Give the extent of all Babesia divergens-infected red blood cells.
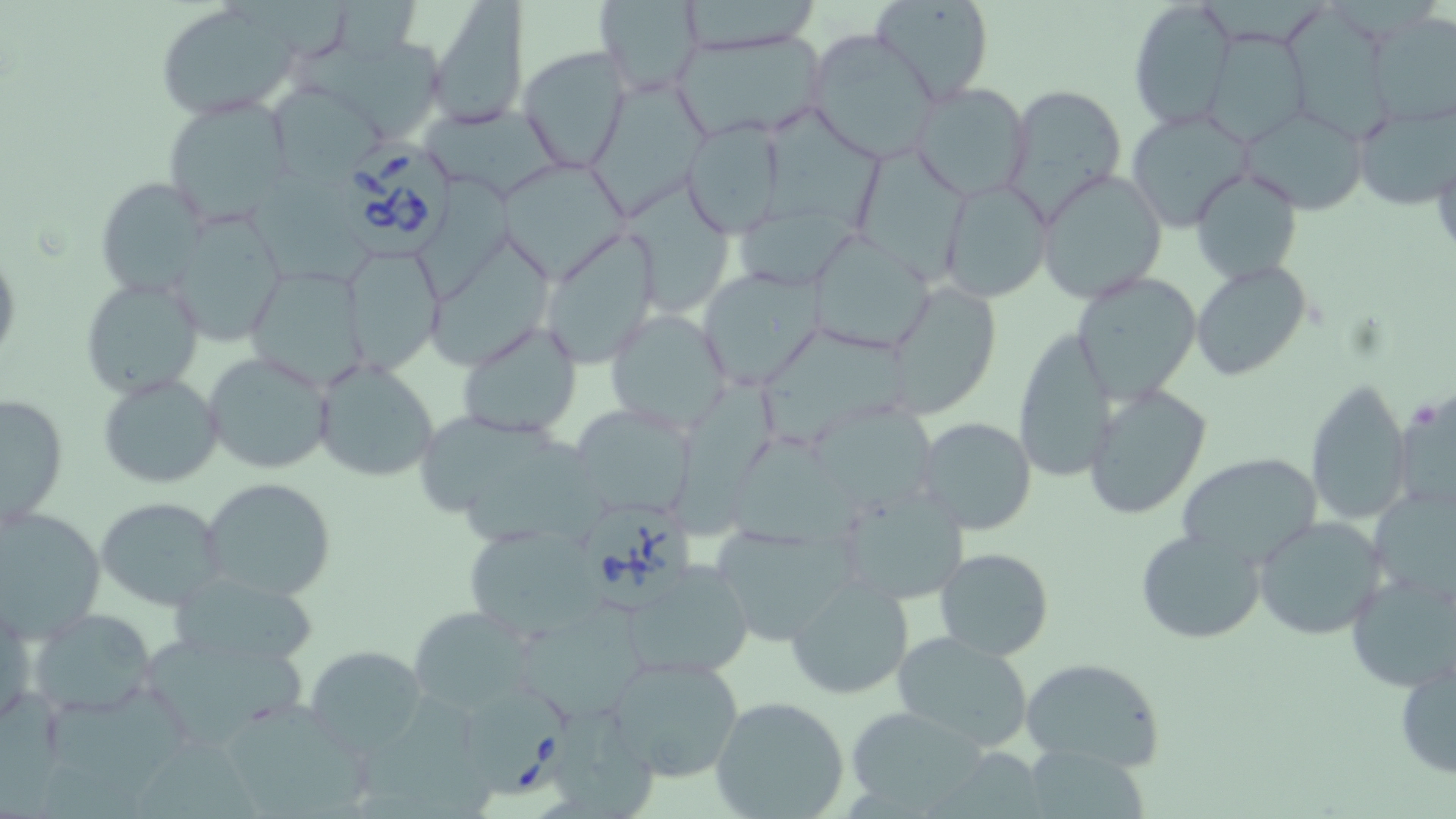
Approximate bounding boxes as (x1,y1)-(x2,y2) corner pairs in pixels.
Babesia divergens-infected red blood cells: (336,137)-(462,262), (580,501)-(702,614), (462,684)-(572,802).

Uninfected red blood cell locations: (427,0)-(530,130), (870,0)-(995,105), (223,1)-(351,59), (594,1)-(705,96), (678,1)-(821,52), (1126,1)-(1237,130), (153,3)-(302,118), (1280,11)-(1391,138), (1365,13)-(1455,127), (1203,29)-(1308,147), (673,30)-(830,141), (807,30)-(941,162), (518,44)-(631,171), (289,51)-(444,135), (269,82)-(387,182), (595,82)-(715,213), (909,82)-(1034,202), (1004,83)-(1128,217), (161,96)-(297,226), (1354,100)-(1455,208), (1239,105)-(1366,214), (1126,107)-(1255,230), (757,108)-(893,224), (682,119)-(785,237), (859,148)-(965,283), (500,158)-(630,278), (1035,168)-(1166,304), (1189,168)-(1304,284), (406,173)-(516,302), (248,175)-(376,288), (95,177)-(210,297), (623,181)-(734,313), (941,181)-(1057,307), (738,206)-(861,294), (164,207)-(289,346), (537,228)-(663,369), (807,230)-(937,355), (427,241)-(553,371), (340,245)-(440,372), (1190,259)-(1313,383), (242,264)-(372,392), (696,268)-(823,389), (1070,269)-(1203,404), (80,276)-(204,400), (882,279)-(1003,418), (626,293)-(816,418), (605,307)-(734,431), (456,322)-(582,441), (1013,327)-(1117,483), (751,328)-(906,453), (202,351)-(334,474), (312,358)-(440,484), (98,374)-(223,489), (670,378)-(779,536), (1304,378)-(1412,527), (1083,384)-(1213,520), (1392,386)-(1456,518), (1,391)-(69,528), (570,402)-(698,519), (811,407)-(943,510), (419,409)-(564,511), (915,416)-(1037,535), (732,437)-(866,546), (1176,453)-(1324,570), (201,476)-(338,601), (832,482)-(971,606), (1368,486)-(1455,603), (95,496)-(227,609), (0,505)-(107,639), (1253,515)-(1391,642), (707,520)-(854,646), (461,524)-(603,639), (1135,528)-(1266,645), (935,547)-(1054,661), (619,558)-(759,681), (1345,568)-(1456,693), (172,571)-(317,671), (786,576)-(914,700), (0,594)-(36,731), (510,601)-(651,721), (412,606)-(539,714), (28,608)-(157,718), (135,626)-(310,751), (892,632)-(1036,754), (306,646)-(427,754), (605,650)-(746,786), (1393,653)-(1455,781), (1019,656)-(1169,772), (355,687)-(477,798), (43,690)-(194,800), (710,694)-(851,819), (554,701)-(657,819), (219,706)-(366,819), (845,708)-(989,813), (135,735)-(271,819), (1029,744)-(1157,819), (929,749)-(1055,819). Platelet locations: (1413,406)-(1440,430). Slide-level diagnosis: Babesia divergens. Light microscopy. Thin blood film. Single field of view. Captured at 1000x magnification. Image is 1456×819 pixels. May-Grünwald-Giemsa stain.